Give the extent of all Plasmodium vivax-infected red blood cells.
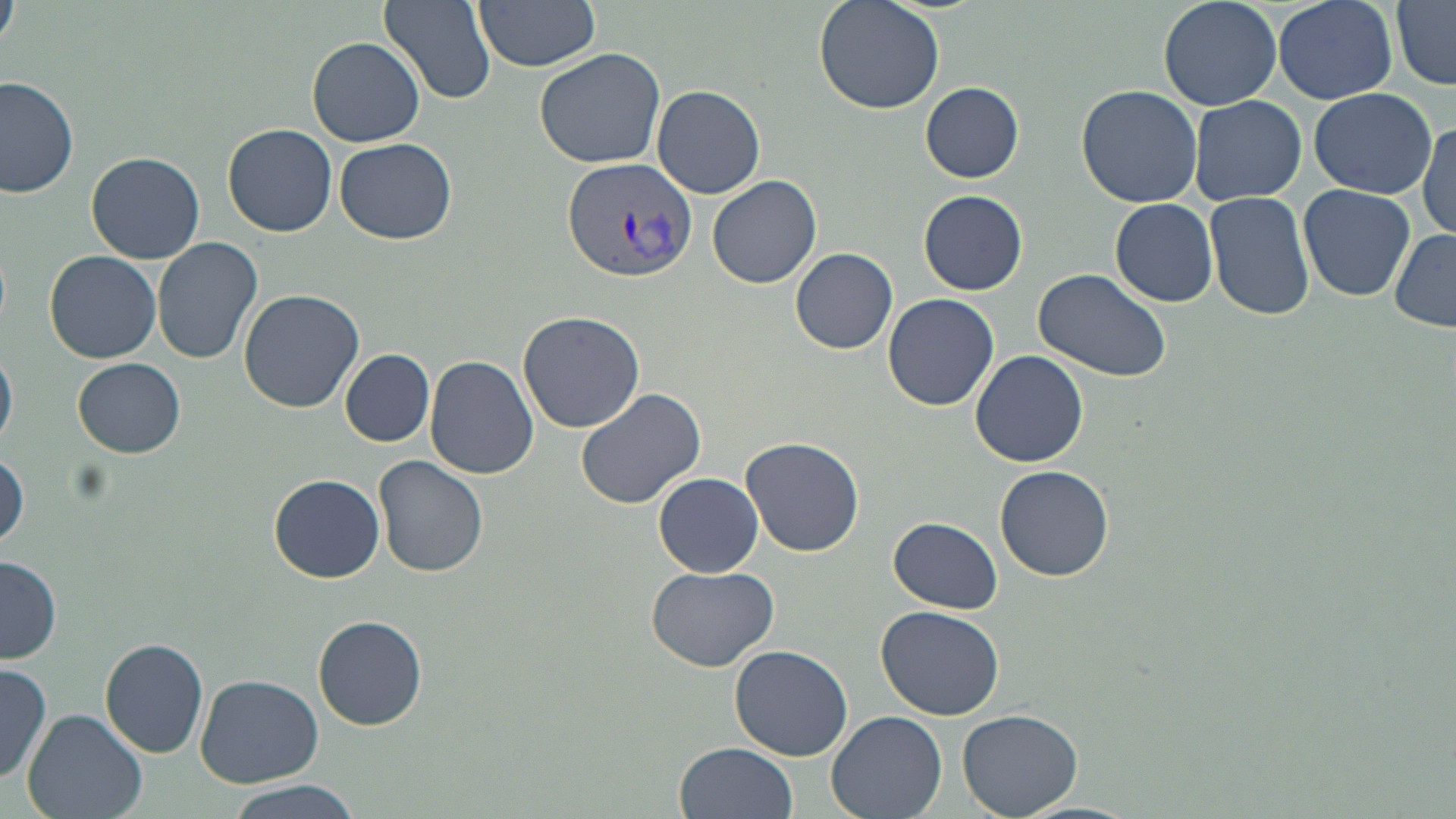
Approximate bounding boxes as [x1, y1, x2, y2] in pixels.
Plasmodium vivax-infected red blood cells: [564, 158, 699, 283].

Uninfected red blood cell locations: [474, 0, 601, 71], [814, 0, 945, 115], [1157, 0, 1285, 112], [1275, 0, 1397, 104], [0, 1, 19, 48], [377, 1, 498, 105], [1392, 1, 1456, 89], [306, 36, 426, 148], [535, 46, 666, 170], [1, 76, 79, 198], [920, 81, 1024, 183], [651, 83, 768, 200], [1077, 84, 1204, 207], [1308, 87, 1436, 199], [1188, 94, 1307, 205], [1416, 115, 1455, 243], [224, 123, 336, 237], [334, 137, 457, 244], [87, 150, 205, 263], [706, 175, 823, 289], [1299, 184, 1415, 302], [918, 189, 1028, 295], [1205, 189, 1316, 320], [1111, 198, 1218, 308], [1390, 228, 1456, 333], [153, 237, 264, 367], [790, 247, 898, 353], [45, 250, 162, 363], [1032, 266, 1173, 384], [239, 288, 365, 412], [881, 292, 1000, 411], [516, 310, 645, 432], [0, 346, 17, 449], [340, 349, 434, 447], [971, 350, 1088, 468], [425, 356, 538, 479], [74, 358, 186, 459], [575, 386, 706, 509], [739, 436, 865, 557], [1, 453, 28, 551], [372, 455, 488, 578], [994, 464, 1113, 581], [654, 473, 764, 577], [270, 474, 386, 582], [888, 516, 1003, 613], [1, 556, 63, 664], [645, 564, 779, 671], [874, 605, 1005, 719], [312, 614, 429, 731], [100, 636, 209, 757], [729, 644, 854, 759], [0, 664, 51, 785], [195, 674, 323, 786], [958, 707, 1082, 818], [22, 710, 147, 819], [827, 711, 947, 819], [675, 741, 798, 819], [219, 779, 366, 819]. Slide-level diagnosis: Plasmodium vivax. Single field of view. May-Grünwald-Giemsa stain. Captured at 1000x magnification. Thin blood smear. Light microscopy. Image is 1456×819 pixels.